Locate every blood parasite and identify its species.
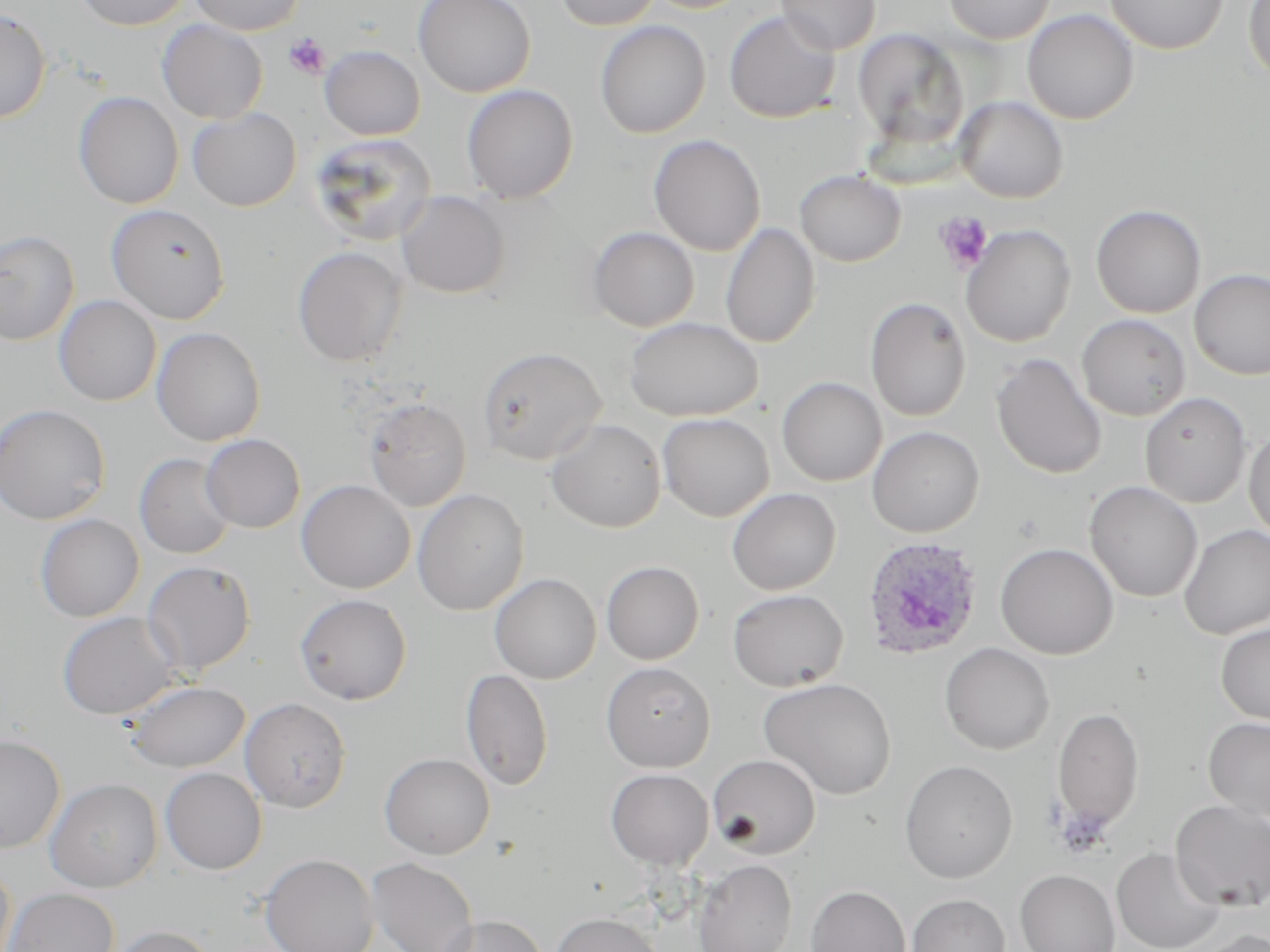
Approximate bounding boxes as named x1/y1/x2/y2 corners in pixels.
Plasmodium ovale-infected red blood cells: (x1=861, y1=536, x2=985, y2=662).
No Plasmodium falciparum, Plasmodium malariae, Plasmodium vivax, Babesia divergens, or Trypanosoma brucei observed.

Summary:
  - Uninfected red blood cell locations: (x1=73, y1=0, x2=193, y2=30), (x1=189, y1=0, x2=306, y2=35), (x1=412, y1=0, x2=535, y2=98), (x1=554, y1=0, x2=662, y2=30), (x1=640, y1=0, x2=756, y2=13), (x1=775, y1=0, x2=881, y2=55), (x1=943, y1=0, x2=1055, y2=44), (x1=1106, y1=0, x2=1228, y2=54), (x1=1243, y1=0, x2=1270, y2=84), (x1=0, y1=8, x2=51, y2=124), (x1=1022, y1=9, x2=1139, y2=124), (x1=723, y1=11, x2=841, y2=123), (x1=157, y1=19, x2=268, y2=123), (x1=595, y1=20, x2=711, y2=138), (x1=853, y1=29, x2=970, y2=149), (x1=319, y1=45, x2=425, y2=140), (x1=461, y1=84, x2=579, y2=203), (x1=74, y1=91, x2=184, y2=209), (x1=955, y1=96, x2=1068, y2=203), (x1=188, y1=107, x2=301, y2=211), (x1=308, y1=133, x2=438, y2=246), (x1=648, y1=134, x2=766, y2=256), (x1=795, y1=169, x2=905, y2=266), (x1=396, y1=191, x2=511, y2=299), (x1=105, y1=204, x2=231, y2=325), (x1=1091, y1=204, x2=1207, y2=318), (x1=720, y1=222, x2=821, y2=349), (x1=961, y1=224, x2=1076, y2=347), (x1=588, y1=226, x2=700, y2=331), (x1=0, y1=229, x2=80, y2=346), (x1=292, y1=245, x2=408, y2=366), (x1=1189, y1=268, x2=1270, y2=379), (x1=53, y1=295, x2=162, y2=406), (x1=865, y1=297, x2=971, y2=422), (x1=1076, y1=314, x2=1191, y2=420), (x1=624, y1=317, x2=763, y2=421), (x1=151, y1=327, x2=265, y2=446), (x1=477, y1=346, x2=607, y2=465), (x1=991, y1=353, x2=1107, y2=479), (x1=777, y1=376, x2=887, y2=486), (x1=1139, y1=391, x2=1251, y2=507), (x1=363, y1=398, x2=472, y2=512), (x1=0, y1=403, x2=111, y2=525), (x1=657, y1=412, x2=774, y2=521), (x1=546, y1=418, x2=666, y2=533), (x1=1244, y1=425, x2=1270, y2=543), (x1=867, y1=426, x2=984, y2=537), (x1=200, y1=434, x2=305, y2=533), (x1=134, y1=453, x2=237, y2=559), (x1=296, y1=480, x2=415, y2=593), (x1=1084, y1=480, x2=1203, y2=602), (x1=727, y1=487, x2=841, y2=595), (x1=412, y1=488, x2=530, y2=615), (x1=35, y1=514, x2=145, y2=622), (x1=1179, y1=524, x2=1270, y2=640), (x1=995, y1=542, x2=1119, y2=660), (x1=142, y1=560, x2=256, y2=675), (x1=601, y1=560, x2=705, y2=664), (x1=489, y1=573, x2=601, y2=684), (x1=728, y1=589, x2=849, y2=691), (x1=294, y1=593, x2=412, y2=705), (x1=57, y1=611, x2=181, y2=720), (x1=1216, y1=623, x2=1270, y2=724), (x1=939, y1=642, x2=1054, y2=755), (x1=600, y1=661, x2=716, y2=771), (x1=461, y1=668, x2=553, y2=790), (x1=759, y1=677, x2=897, y2=799), (x1=123, y1=680, x2=251, y2=773), (x1=240, y1=698, x2=351, y2=812), (x1=1052, y1=705, x2=1145, y2=832), (x1=1202, y1=717, x2=1270, y2=823), (x1=0, y1=734, x2=66, y2=852), (x1=379, y1=752, x2=495, y2=859), (x1=707, y1=754, x2=821, y2=859), (x1=899, y1=760, x2=1018, y2=883), (x1=160, y1=767, x2=267, y2=874), (x1=606, y1=768, x2=714, y2=869), (x1=44, y1=778, x2=163, y2=892), (x1=1170, y1=800, x2=1270, y2=911), (x1=1111, y1=847, x2=1226, y2=952), (x1=259, y1=853, x2=379, y2=952), (x1=367, y1=856, x2=480, y2=952), (x1=692, y1=859, x2=796, y2=952), (x1=0, y1=860, x2=15, y2=952), (x1=1015, y1=869, x2=1120, y2=952), (x1=805, y1=884, x2=911, y2=952), (x1=2, y1=887, x2=120, y2=952), (x1=907, y1=894, x2=1010, y2=952), (x1=549, y1=912, x2=665, y2=952), (x1=436, y1=914, x2=548, y2=952), (x1=107, y1=925, x2=218, y2=952), (x1=1192, y1=930, x2=1270, y2=952)
  - Platelet locations: (x1=284, y1=33, x2=331, y2=79), (x1=934, y1=212, x2=994, y2=273), (x1=1053, y1=804, x2=1114, y2=859)
  - Slide-level diagnosis: Plasmodium ovale
  - Magnification: 1000x
  - Image size: 1270×952 pixels
  - Modality: light microscopy
  - Preparation: thin blood film
  - Stain: May-Grünwald-Giemsa
  - Field of view: single